Assess this cell for malaria.
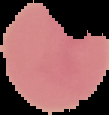

Uninfected.

image_size: 109×115 pixels
preparation: thin blood smear
image_type: segmented cell region with the area outside set to black